Report the malaria status of this cell.
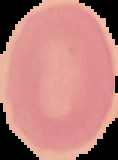

It is uninfected.

Summary:
  - Image type: cell region segmented out of the field of view; surrounding area masked to black
  - Image size: 118×160 pixels
  - Preparation: thin blood smear